Identify the blood parasite species.
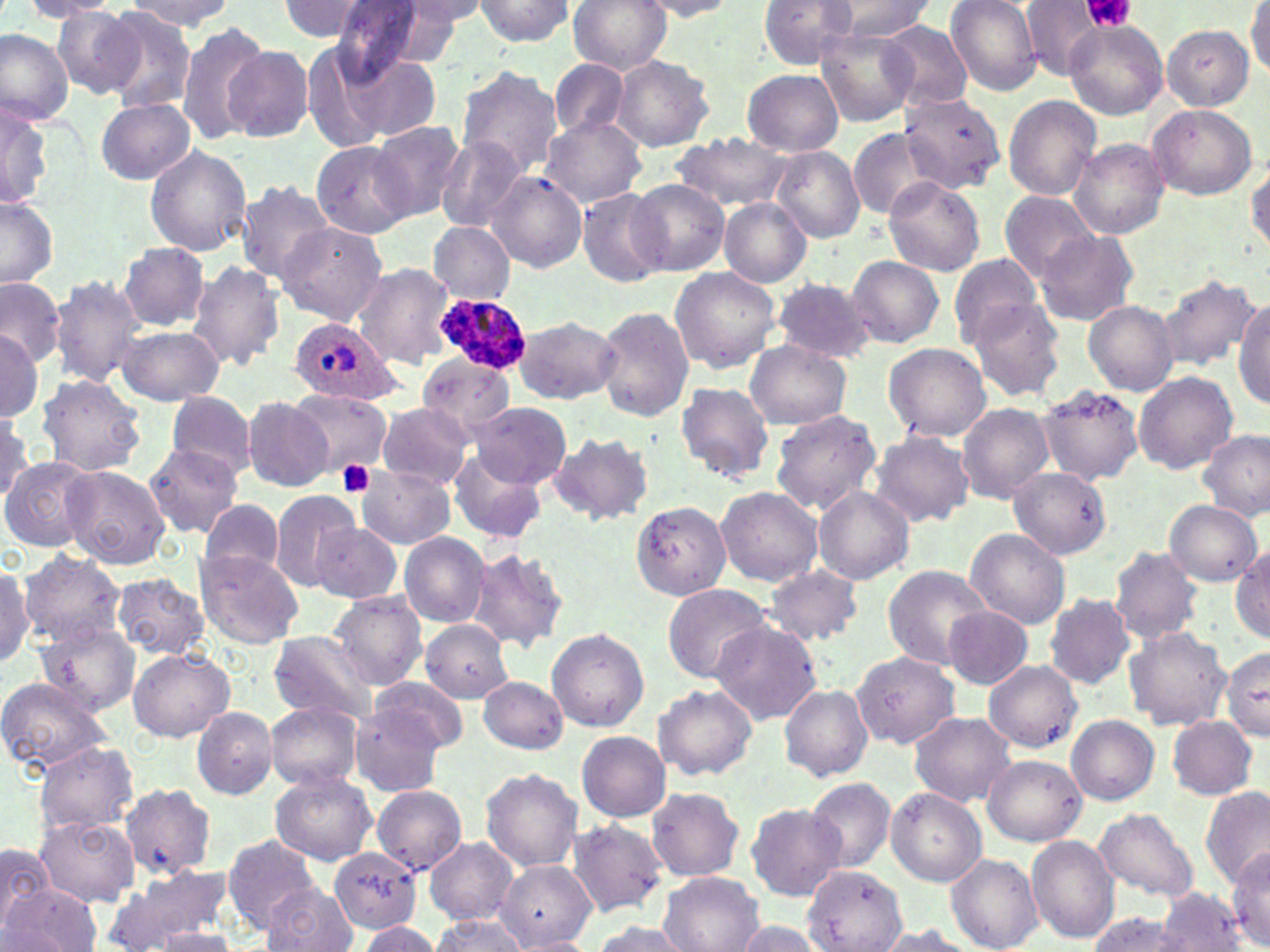
Plasmodium ovale.

Approximate bounding boxes as named x1/y1/x2/y2 corners in pixels. Plasmodium ovale-infected red blood cell locations: (x1=435, y1=296, x2=531, y2=370), (x1=289, y1=317, x2=399, y2=406). Uninfected red blood cell locations: (x1=23, y1=0, x2=123, y2=19), (x1=124, y1=0, x2=232, y2=32), (x1=471, y1=0, x2=577, y2=46), (x1=567, y1=0, x2=671, y2=74), (x1=637, y1=0, x2=742, y2=20), (x1=759, y1=0, x2=860, y2=69), (x1=829, y1=0, x2=933, y2=41), (x1=945, y1=0, x2=1044, y2=95), (x1=1018, y1=0, x2=1117, y2=81), (x1=277, y1=1, x2=379, y2=42), (x1=398, y1=1, x2=493, y2=32), (x1=327, y1=2, x2=449, y2=79), (x1=765, y1=2, x2=923, y2=93), (x1=1247, y1=3, x2=1270, y2=78), (x1=54, y1=8, x2=145, y2=97), (x1=100, y1=8, x2=196, y2=111), (x1=878, y1=19, x2=975, y2=108), (x1=176, y1=20, x2=271, y2=147), (x1=1063, y1=20, x2=1168, y2=120), (x1=1161, y1=25, x2=1255, y2=110), (x1=0, y1=28, x2=73, y2=126), (x1=818, y1=29, x2=919, y2=125), (x1=224, y1=46, x2=312, y2=142), (x1=339, y1=55, x2=442, y2=143), (x1=610, y1=55, x2=715, y2=152), (x1=548, y1=60, x2=630, y2=142), (x1=454, y1=64, x2=563, y2=179), (x1=743, y1=69, x2=843, y2=157), (x1=896, y1=88, x2=1009, y2=192), (x1=1, y1=95, x2=53, y2=211), (x1=1004, y1=95, x2=1101, y2=201), (x1=96, y1=99, x2=195, y2=184), (x1=1146, y1=102, x2=1257, y2=199), (x1=540, y1=116, x2=646, y2=208), (x1=369, y1=121, x2=468, y2=222), (x1=849, y1=127, x2=943, y2=220), (x1=670, y1=131, x2=797, y2=213), (x1=437, y1=136, x2=526, y2=229), (x1=1069, y1=138, x2=1169, y2=240), (x1=311, y1=140, x2=417, y2=239), (x1=144, y1=145, x2=253, y2=256), (x1=771, y1=147, x2=865, y2=243), (x1=1247, y1=162, x2=1270, y2=253), (x1=487, y1=170, x2=587, y2=273), (x1=882, y1=176, x2=985, y2=277), (x1=238, y1=180, x2=335, y2=282), (x1=629, y1=180, x2=730, y2=275), (x1=576, y1=188, x2=671, y2=286), (x1=999, y1=190, x2=1100, y2=283), (x1=0, y1=196, x2=59, y2=289), (x1=719, y1=198, x2=812, y2=288), (x1=274, y1=222, x2=387, y2=326), (x1=430, y1=223, x2=516, y2=302), (x1=1034, y1=230, x2=1139, y2=327), (x1=117, y1=245, x2=212, y2=331), (x1=947, y1=253, x2=1042, y2=349), (x1=846, y1=255, x2=944, y2=349), (x1=187, y1=262, x2=286, y2=371), (x1=351, y1=262, x2=454, y2=367), (x1=669, y1=265, x2=781, y2=373), (x1=50, y1=274, x2=146, y2=387), (x1=1157, y1=274, x2=1259, y2=371), (x1=0, y1=277, x2=65, y2=367), (x1=772, y1=279, x2=876, y2=363), (x1=1234, y1=298, x2=1270, y2=411), (x1=967, y1=299, x2=1069, y2=402), (x1=1083, y1=302, x2=1179, y2=395), (x1=596, y1=306, x2=695, y2=422), (x1=513, y1=314, x2=621, y2=403), (x1=114, y1=326, x2=224, y2=405), (x1=0, y1=330, x2=44, y2=420), (x1=744, y1=341, x2=851, y2=430), (x1=883, y1=342, x2=990, y2=441), (x1=752, y1=349, x2=870, y2=489), (x1=419, y1=354, x2=516, y2=438), (x1=1133, y1=371, x2=1238, y2=474), (x1=36, y1=373, x2=147, y2=476), (x1=675, y1=381, x2=774, y2=484), (x1=1036, y1=384, x2=1145, y2=486), (x1=288, y1=388, x2=392, y2=480), (x1=167, y1=390, x2=255, y2=477), (x1=243, y1=396, x2=336, y2=493), (x1=374, y1=402, x2=474, y2=488), (x1=470, y1=403, x2=570, y2=488), (x1=957, y1=404, x2=1054, y2=503), (x1=769, y1=408, x2=882, y2=516), (x1=0, y1=409, x2=43, y2=497), (x1=868, y1=430, x2=975, y2=526), (x1=1198, y1=430, x2=1269, y2=519), (x1=548, y1=432, x2=655, y2=524), (x1=145, y1=443, x2=243, y2=536), (x1=447, y1=448, x2=548, y2=543), (x1=1, y1=456, x2=97, y2=552), (x1=61, y1=464, x2=170, y2=569), (x1=357, y1=466, x2=453, y2=549), (x1=1011, y1=467, x2=1111, y2=558), (x1=716, y1=485, x2=823, y2=585), (x1=811, y1=487, x2=914, y2=585), (x1=267, y1=489, x2=361, y2=590), (x1=629, y1=500, x2=731, y2=600), (x1=1165, y1=500, x2=1262, y2=587), (x1=197, y1=503, x2=286, y2=577), (x1=310, y1=520, x2=403, y2=604), (x1=963, y1=527, x2=1071, y2=629), (x1=397, y1=532, x2=491, y2=627), (x1=1109, y1=545, x2=1204, y2=645), (x1=1232, y1=545, x2=1270, y2=641), (x1=465, y1=548, x2=569, y2=653), (x1=194, y1=550, x2=303, y2=648), (x1=19, y1=551, x2=125, y2=647), (x1=0, y1=560, x2=33, y2=669), (x1=882, y1=565, x2=992, y2=669), (x1=763, y1=566, x2=863, y2=646), (x1=109, y1=572, x2=211, y2=660), (x1=662, y1=582, x2=776, y2=683), (x1=328, y1=592, x2=427, y2=689), (x1=1043, y1=592, x2=1137, y2=689), (x1=944, y1=605, x2=1034, y2=689), (x1=420, y1=620, x2=511, y2=703), (x1=709, y1=620, x2=823, y2=724), (x1=37, y1=624, x2=139, y2=715), (x1=1123, y1=626, x2=1231, y2=730), (x1=547, y1=628, x2=648, y2=731), (x1=267, y1=631, x2=378, y2=723), (x1=1221, y1=646, x2=1270, y2=741), (x1=128, y1=648, x2=234, y2=742), (x1=851, y1=650, x2=959, y2=748), (x1=983, y1=660, x2=1083, y2=752), (x1=0, y1=676, x2=111, y2=773), (x1=478, y1=676, x2=567, y2=754), (x1=368, y1=677, x2=471, y2=757), (x1=779, y1=683, x2=875, y2=782), (x1=652, y1=684, x2=758, y2=781), (x1=265, y1=701, x2=363, y2=791), (x1=191, y1=706, x2=278, y2=799), (x1=349, y1=706, x2=449, y2=797), (x1=908, y1=711, x2=1017, y2=806), (x1=1067, y1=714, x2=1160, y2=804), (x1=1167, y1=714, x2=1258, y2=800), (x1=577, y1=731, x2=669, y2=821), (x1=34, y1=742, x2=139, y2=835), (x1=983, y1=754, x2=1086, y2=847), (x1=479, y1=767, x2=583, y2=873), (x1=269, y1=770, x2=377, y2=865), (x1=806, y1=778, x2=894, y2=872), (x1=371, y1=784, x2=468, y2=875), (x1=119, y1=785, x2=216, y2=879), (x1=1202, y1=786, x2=1270, y2=892), (x1=647, y1=787, x2=745, y2=881), (x1=886, y1=787, x2=987, y2=885), (x1=746, y1=803, x2=845, y2=901), (x1=1093, y1=808, x2=1200, y2=903), (x1=35, y1=815, x2=139, y2=907), (x1=567, y1=818, x2=668, y2=917), (x1=223, y1=834, x2=320, y2=931), (x1=1026, y1=835, x2=1119, y2=944), (x1=425, y1=837, x2=517, y2=924), (x1=0, y1=843, x2=52, y2=929), (x1=1229, y1=847, x2=1270, y2=949), (x1=329, y1=848, x2=422, y2=935), (x1=946, y1=853, x2=1042, y2=952), (x1=497, y1=862, x2=596, y2=949), (x1=114, y1=863, x2=229, y2=945), (x1=804, y1=864, x2=908, y2=950), (x1=658, y1=872, x2=764, y2=952), (x1=5, y1=884, x2=101, y2=952), (x1=263, y1=884, x2=356, y2=951), (x1=1157, y1=888, x2=1244, y2=951), (x1=1087, y1=912, x2=1184, y2=951), (x1=431, y1=914, x2=532, y2=951), (x1=731, y1=919, x2=826, y2=952), (x1=355, y1=921, x2=443, y2=951), (x1=590, y1=921, x2=692, y2=952), (x1=870, y1=924, x2=988, y2=952), (x1=154, y1=929, x2=240, y2=951), (x1=510, y1=935, x2=598, y2=952). Platelet locations: (x1=1078, y1=0, x2=1136, y2=32), (x1=337, y1=461, x2=375, y2=498). May-Grünwald-Giemsa stain. Optical microscopy. 1000x magnification. Image is 1270×952 pixels. One field of a larger specimen. Thin blood film.